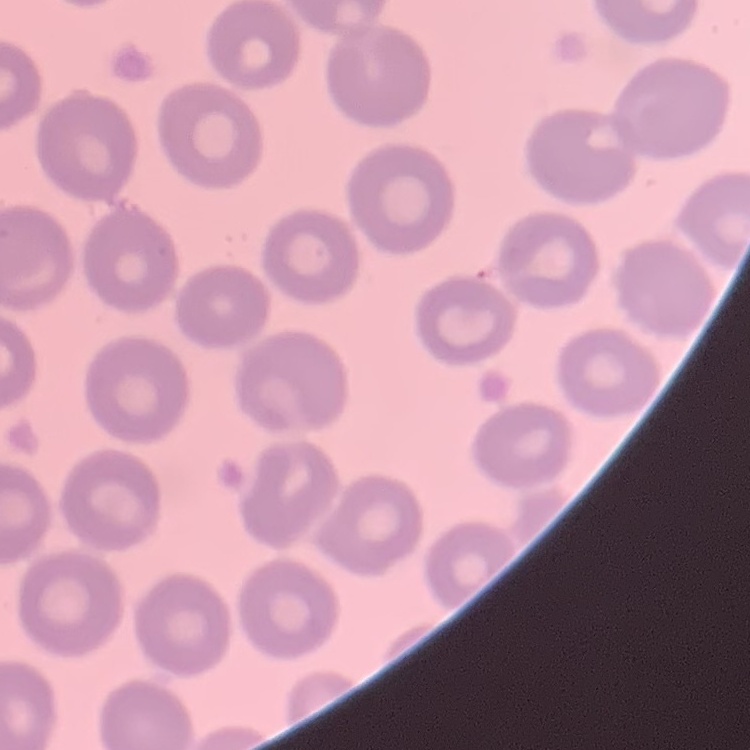
Summary:
  - Red blood cell morphology: no rouleaux formation
  - Preparation: thin blood film
  - Stain: Field's or Giemsa
  - Image type: one tile cut from a larger photomicrograph